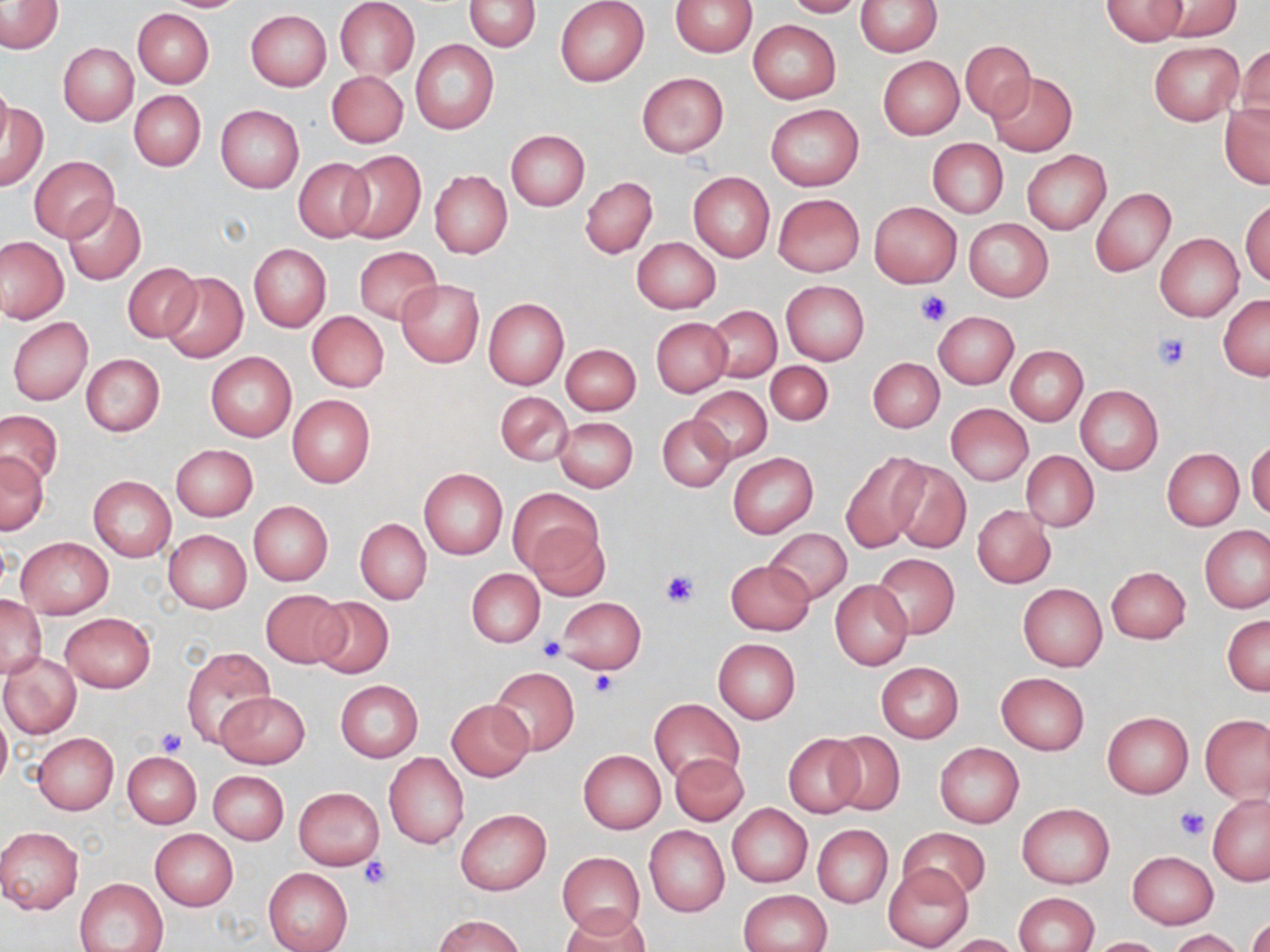
Summary:
  - Coordinate format: approximate bounding boxes as [x1, y1, x2, y2] in pixels
  - Platelet locations: [914, 289, 955, 327], [1153, 331, 1192, 370], [661, 570, 699, 607], [539, 637, 566, 662], [589, 670, 620, 699], [157, 727, 186, 757], [1175, 807, 1210, 839], [362, 856, 390, 888]
  - Uninfected red blood cell locations: [157, 0, 249, 12], [335, 0, 419, 80], [464, 0, 541, 51], [555, 0, 648, 86], [670, 0, 757, 57], [783, 0, 862, 18], [1101, 0, 1189, 44], [1157, 0, 1243, 38], [1, 1, 63, 53], [857, 1, 941, 55], [133, 8, 214, 88], [246, 10, 331, 91], [749, 20, 841, 103], [410, 39, 499, 134], [960, 39, 1035, 121], [1149, 41, 1243, 125], [59, 43, 138, 125], [1233, 47, 1269, 134], [878, 55, 964, 140], [327, 70, 408, 148], [637, 72, 728, 157], [987, 72, 1077, 156], [0, 78, 12, 156], [129, 90, 205, 171], [1, 102, 49, 190], [1220, 103, 1269, 189], [765, 104, 864, 192], [216, 105, 303, 192], [505, 130, 590, 210], [927, 139, 1008, 218], [341, 150, 425, 243], [1022, 150, 1111, 233], [30, 156, 119, 241], [292, 156, 375, 243], [430, 171, 512, 258], [688, 172, 775, 262], [580, 177, 657, 258], [1090, 186, 1175, 276], [773, 194, 865, 277], [63, 198, 146, 285], [1242, 199, 1269, 287], [869, 202, 960, 287], [964, 218, 1054, 301], [1155, 233, 1244, 320], [1, 237, 68, 323], [632, 237, 720, 313], [249, 244, 331, 331], [354, 247, 442, 323], [123, 263, 200, 342], [161, 272, 248, 362], [397, 279, 484, 366], [781, 280, 869, 366], [1219, 295, 1270, 380], [484, 298, 569, 389], [704, 306, 781, 383], [307, 311, 389, 393], [934, 311, 1019, 388], [8, 317, 93, 406], [651, 317, 732, 397], [560, 342, 641, 416], [1006, 345, 1088, 426], [206, 352, 296, 441], [82, 354, 164, 436], [868, 357, 944, 433], [765, 361, 832, 427], [688, 385, 772, 463], [1075, 386, 1163, 476], [496, 391, 573, 467], [287, 395, 375, 487], [947, 404, 1032, 484], [0, 408, 65, 486], [657, 414, 734, 492], [554, 417, 638, 492], [1247, 441, 1270, 520], [171, 444, 258, 520], [1163, 448, 1244, 530], [1020, 450, 1099, 532], [840, 451, 929, 553], [728, 452, 818, 539], [1, 453, 49, 533], [888, 460, 971, 553], [419, 467, 508, 559], [88, 475, 176, 562], [508, 488, 602, 579], [248, 501, 332, 586], [972, 504, 1055, 588], [355, 518, 431, 604], [527, 523, 610, 601], [1201, 525, 1269, 612], [763, 528, 851, 604], [163, 529, 251, 612], [16, 536, 113, 618], [872, 554, 960, 639], [725, 560, 814, 635], [1106, 565, 1191, 643], [467, 569, 544, 646], [830, 579, 912, 671], [1018, 584, 1107, 672], [259, 589, 349, 669], [0, 594, 45, 678], [308, 596, 394, 679], [558, 597, 645, 673], [60, 613, 156, 692], [1223, 615, 1269, 695], [714, 638, 801, 724], [181, 648, 272, 747], [0, 654, 81, 738], [876, 661, 963, 743], [491, 667, 580, 756], [997, 672, 1089, 755], [335, 681, 423, 762], [215, 691, 311, 768], [649, 698, 744, 782], [447, 699, 533, 781], [0, 708, 11, 791], [1102, 711, 1193, 798], [1201, 713, 1269, 802], [827, 731, 905, 816], [32, 733, 119, 814], [784, 734, 864, 817], [934, 742, 1024, 828], [579, 750, 666, 833], [123, 751, 202, 828], [384, 752, 470, 849], [671, 753, 747, 825], [209, 771, 289, 845], [293, 787, 384, 868], [1207, 793, 1270, 885], [1017, 803, 1114, 888], [727, 804, 812, 887], [456, 809, 551, 896], [813, 824, 893, 907], [644, 826, 729, 917], [899, 826, 989, 903], [0, 827, 83, 915], [150, 829, 238, 910], [558, 851, 644, 937], [1127, 851, 1218, 929], [882, 863, 974, 952], [262, 867, 351, 952], [75, 877, 168, 952], [739, 889, 832, 952], [1014, 892, 1099, 952], [562, 908, 650, 952], [436, 915, 522, 952], [1248, 917, 1269, 952], [1168, 929, 1249, 952], [945, 934, 1021, 952], [1087, 937, 1168, 951]
  - Slide-level diagnosis: no evidence of blood parasites
  - Magnification: 1000x
  - Image size: 1270×952 pixels
  - Preparation: thin blood film
  - Stain: May-Grünwald-Giemsa
  - Field of view: one of a larger specimen
  - Modality: optical microscopy